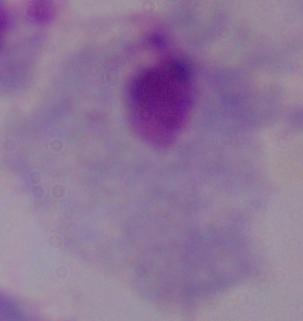
Summary:
  - Identification: trichomonad
  - Magnification: 1000x
  - Modality: micrograph